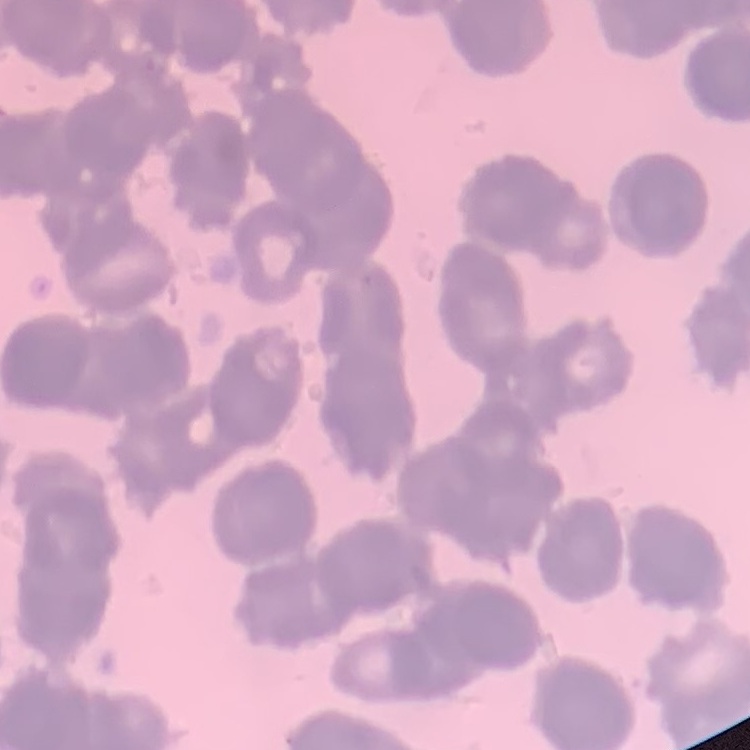

red blood cell morphology = rouleaux formation
stain = Field's or Giemsa
image type = square crop of a larger photomicrograph
preparation = thin blood film